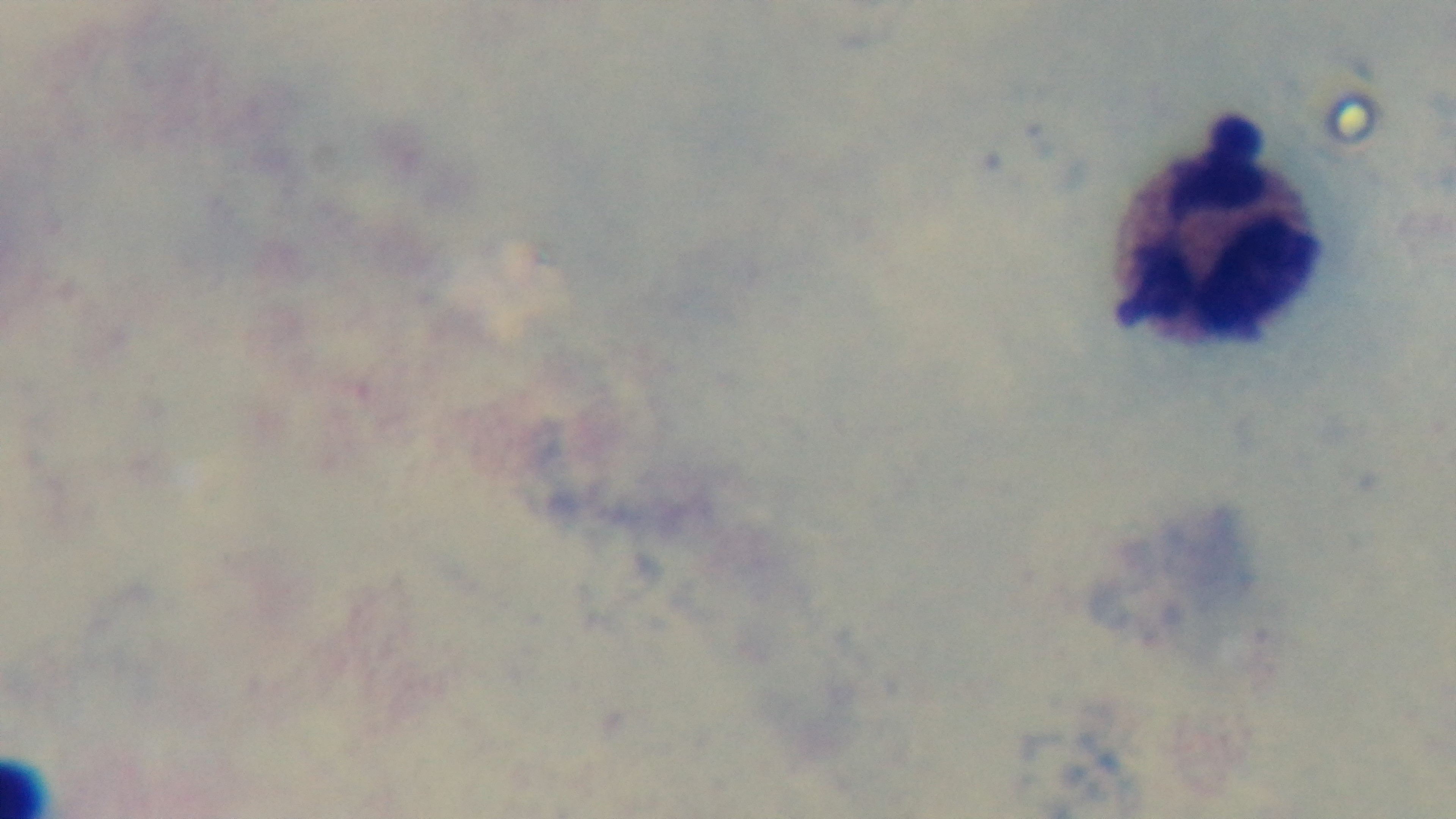

stain = Giemsa
field of view = one from the slide
capture = mounted 4K digital camera
malaria status = uninfected
objective = 100x oil immersion
preparation = thick
modality = light microscopy